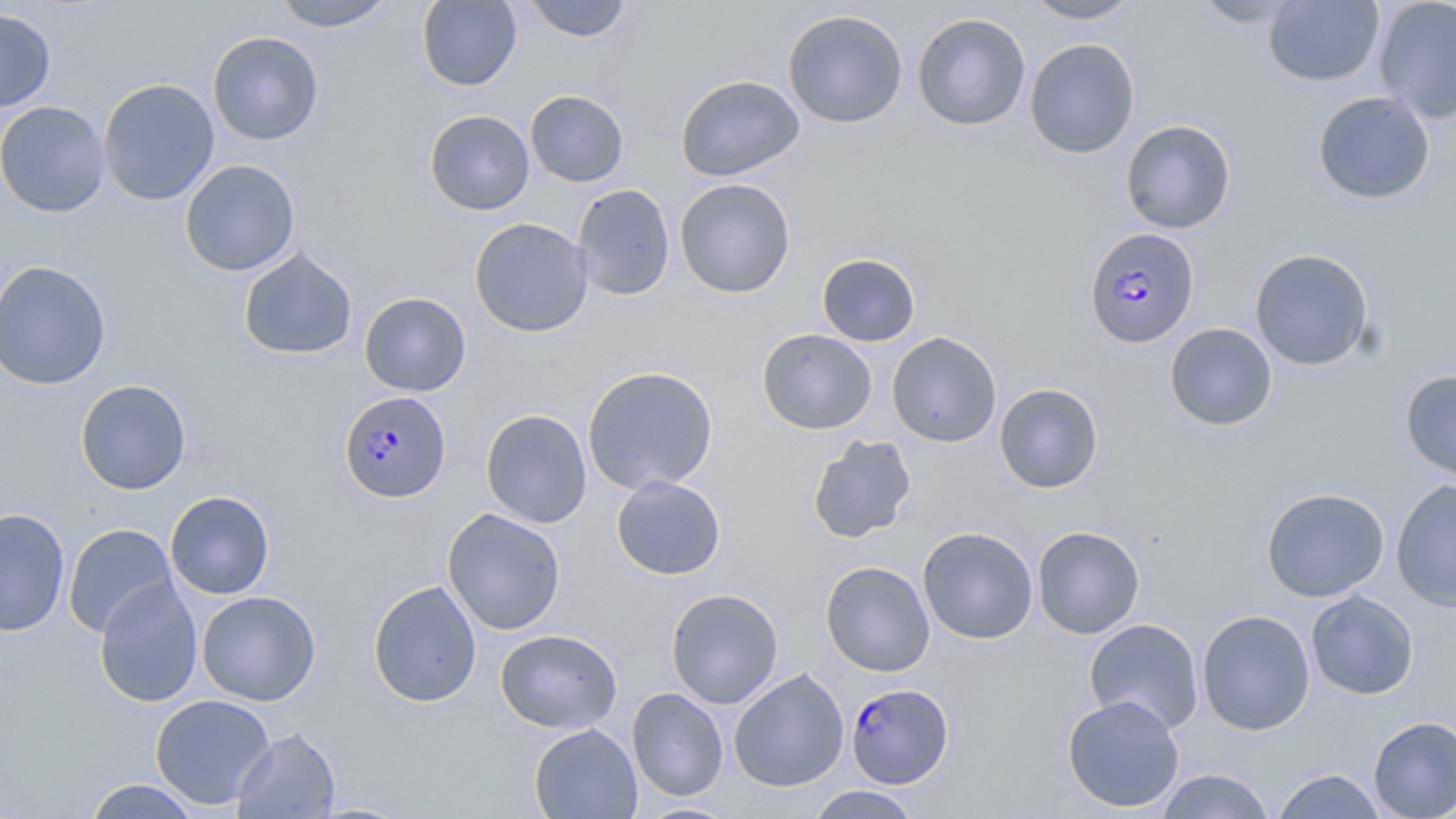
Summary:
  - Coordinate format: approximate bounding boxes as (x1, y1, x2, y2) in pixels
  - Uninfected red blood cell locations: (270, 0, 395, 32), (417, 0, 521, 91), (520, 0, 633, 43), (1023, 0, 1143, 24), (1189, 0, 1311, 28), (1263, 0, 1384, 86), (1373, 0, 1456, 124), (0, 6, 57, 113), (782, 9, 908, 128), (912, 12, 1031, 132), (208, 31, 324, 146), (1024, 38, 1140, 159), (675, 74, 806, 182), (98, 78, 220, 206), (525, 90, 629, 188), (1312, 91, 1435, 205), (0, 100, 110, 218), (424, 110, 535, 215), (1120, 119, 1236, 234), (179, 159, 301, 277), (674, 178, 796, 298), (571, 183, 676, 300), (469, 217, 594, 338), (237, 247, 358, 360), (1250, 248, 1375, 371), (816, 252, 921, 347), (0, 260, 112, 390), (359, 292, 471, 396), (1164, 323, 1278, 431), (757, 328, 877, 434), (886, 332, 1002, 447), (582, 365, 719, 494), (1400, 369, 1456, 483), (75, 379, 192, 495), (994, 383, 1104, 493), (480, 408, 592, 528), (807, 434, 917, 544), (611, 475, 726, 580), (1391, 479, 1456, 613), (1260, 487, 1390, 602), (165, 490, 275, 599), (0, 508, 71, 636), (442, 508, 566, 635), (63, 523, 178, 638), (1032, 525, 1145, 639), (917, 526, 1039, 644), (820, 560, 935, 677), (94, 577, 204, 708), (368, 579, 483, 708), (665, 588, 784, 709), (196, 590, 320, 706), (1306, 591, 1419, 700), (1196, 609, 1316, 735), (1083, 618, 1204, 735), (495, 628, 622, 734), (728, 668, 849, 792), (627, 687, 729, 801), (150, 694, 276, 809), (1061, 694, 1185, 813), (1368, 715, 1456, 818), (528, 723, 643, 818), (231, 727, 342, 819), (1155, 768, 1277, 818), (1271, 768, 1388, 818), (84, 779, 202, 818), (804, 785, 924, 818), (633, 801, 741, 818)
  - Plasmodium falciparum-infected red blood cell locations: (1084, 228, 1200, 349), (339, 390, 451, 503), (846, 683, 953, 787)
  - Slide-level diagnosis: Plasmodium falciparum
  - Image size: 1456×819 pixels
  - Modality: optical microscopy
  - Stain: May-Grünwald-Giemsa
  - Field of view: single
  - Preparation: thin blood smear
  - Magnification: 1000x